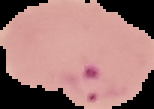

Summary:
  - Image size: 154×109 pixels
  - Preparation: thin blood film
  - Malaria status: parasitized
  - Image type: segmented cell region with the area outside set to black